Name the blood parasite species.
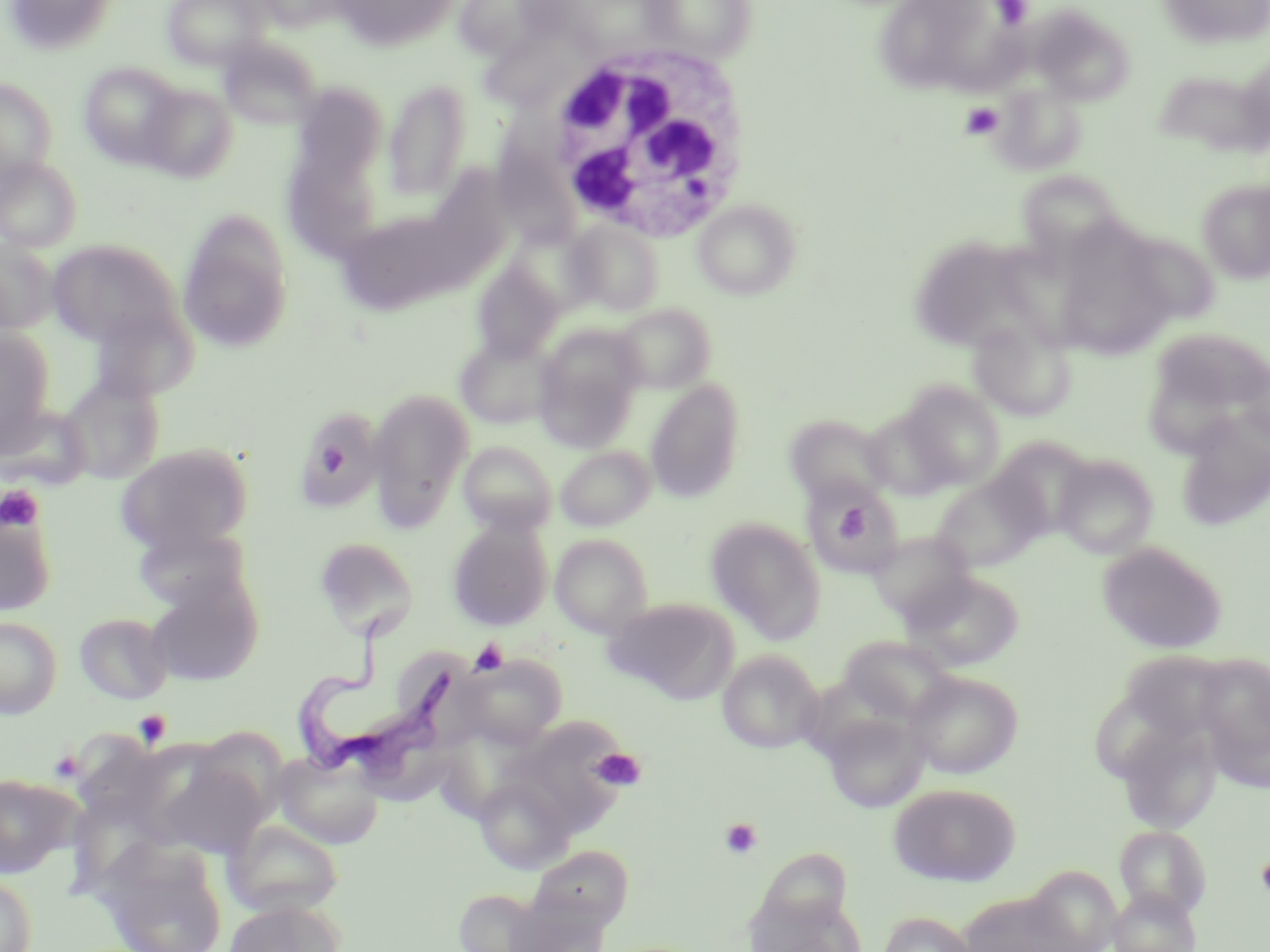
Trypanosoma brucei.

Approximate bounding boxes as (x1, y1, x2, y2) in pixels. Trypanosoma brucei locations: (289, 616, 457, 786). Platelet locations: (992, 0, 1032, 29), (961, 102, 1004, 140), (0, 485, 44, 532), (827, 495, 876, 550), (470, 638, 508, 676), (133, 709, 171, 749), (48, 749, 84, 784), (591, 749, 646, 791), (719, 818, 762, 859), (1256, 853, 1270, 898). Uninfected red blood cell locations: (2, 0, 119, 56), (162, 0, 269, 70), (249, 0, 346, 32), (329, 0, 464, 51), (640, 0, 757, 62), (872, 0, 1021, 99), (1157, 0, 1270, 49), (461, 4, 546, 58), (1030, 6, 1134, 105), (483, 31, 567, 109), (217, 35, 322, 131), (78, 62, 184, 167), (1152, 67, 1267, 158), (0, 78, 58, 185), (383, 79, 473, 205), (990, 81, 1087, 175), (139, 84, 238, 183), (291, 92, 385, 178), (0, 155, 83, 253), (288, 158, 386, 259), (428, 164, 512, 286), (1016, 170, 1128, 260), (1198, 179, 1270, 283), (693, 198, 801, 301), (177, 208, 294, 354), (343, 216, 446, 316), (566, 220, 665, 315), (1053, 227, 1180, 360), (1120, 230, 1221, 325), (908, 233, 1041, 353), (0, 238, 59, 333), (47, 239, 182, 346), (471, 257, 564, 363), (86, 302, 195, 403), (613, 304, 715, 392), (968, 316, 1077, 422), (534, 326, 645, 451), (1147, 327, 1270, 421), (0, 329, 56, 446), (455, 335, 554, 430), (1236, 356, 1270, 450), (59, 374, 165, 484), (646, 380, 745, 503), (896, 381, 1005, 489), (367, 387, 474, 526), (291, 404, 386, 513), (0, 405, 90, 489), (861, 406, 961, 500), (1175, 412, 1270, 531), (784, 413, 893, 504), (988, 436, 1097, 539), (458, 441, 557, 535), (115, 443, 254, 554), (556, 446, 655, 531), (1053, 454, 1159, 558), (932, 473, 1044, 573), (800, 477, 902, 578), (0, 508, 57, 615), (447, 517, 553, 630), (706, 518, 825, 643), (131, 525, 251, 614), (867, 530, 975, 623), (550, 533, 653, 638), (314, 537, 418, 640), (1097, 542, 1228, 654), (906, 569, 1024, 671), (146, 577, 262, 686), (604, 597, 739, 704), (74, 612, 174, 705), (0, 617, 62, 719), (836, 635, 956, 723), (1120, 648, 1223, 729), (717, 649, 824, 753), (1196, 653, 1270, 770), (461, 655, 566, 749), (904, 670, 1023, 779), (821, 710, 929, 813), (514, 717, 631, 833), (1117, 723, 1223, 834), (272, 750, 385, 849), (157, 756, 265, 859), (0, 773, 80, 879), (474, 777, 575, 874), (888, 783, 1022, 887), (223, 818, 344, 917), (1114, 825, 1212, 919), (93, 837, 228, 952), (529, 844, 634, 927), (0, 872, 38, 952), (1022, 873, 1120, 950), (454, 888, 548, 951), (1108, 888, 1201, 952), (958, 890, 1085, 952), (506, 896, 610, 952), (224, 899, 343, 952), (876, 912, 980, 952). White blood cell locations: (543, 40, 753, 244). Optical microscopy. May-Grünwald-Giemsa stain. Image is 1270×952 pixels. Thin blood film. Single field of view. 1000x magnification.